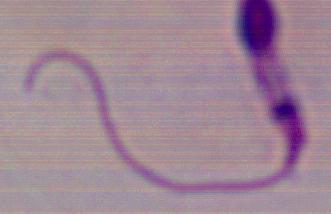 Captured at 1000x magnification. A Leishmania parasite is shown. Photomicrograph.